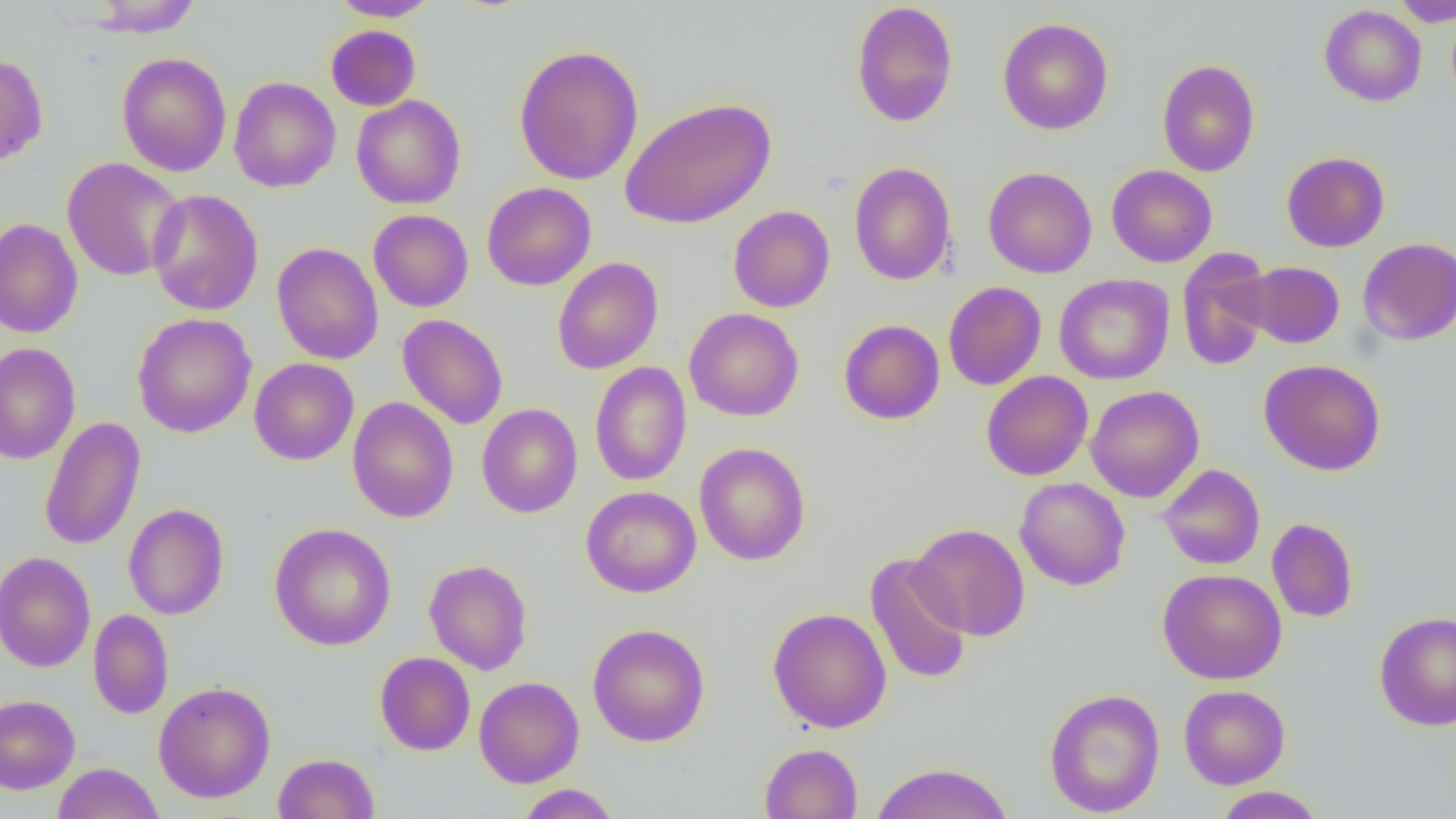

slide-level diagnosis = negative for blood parasites
image size = 1456×819 pixels
uninfected red blood cell locations = approximate bounding boxes as (x1, y1, x2, y2) in pixels: (86, 0, 202, 37), (329, 0, 440, 21), (1390, 0, 1456, 27), (850, 1, 958, 128), (1319, 4, 1427, 106), (997, 17, 1113, 135), (325, 25, 421, 111), (513, 44, 644, 185), (116, 51, 232, 177), (0, 53, 48, 169), (1157, 59, 1260, 177), (228, 77, 341, 192), (351, 95, 465, 210), (619, 96, 776, 230), (1281, 151, 1390, 252), (62, 157, 185, 281), (848, 161, 957, 286), (1106, 165, 1217, 267), (983, 166, 1097, 279), (482, 182, 596, 291), (147, 189, 263, 316), (728, 205, 835, 312), (368, 209, 473, 312), (0, 218, 84, 338), (1357, 237, 1456, 345), (271, 242, 384, 364), (1177, 248, 1275, 371), (552, 257, 663, 375), (1241, 261, 1344, 348), (1054, 274, 1175, 384), (943, 281, 1047, 390), (684, 307, 804, 422), (132, 313, 257, 438), (397, 314, 508, 429), (839, 319, 945, 425), (0, 342, 81, 465), (249, 358, 359, 465), (1258, 358, 1386, 476), (590, 361, 692, 486), (981, 371, 1093, 481), (1085, 385, 1204, 503), (347, 397, 459, 523), (476, 404, 583, 518), (39, 416, 146, 551), (694, 442, 811, 566), (1157, 464, 1265, 570), (1014, 477, 1130, 591), (580, 486, 701, 598), (123, 503, 229, 620), (1267, 517, 1359, 623), (269, 522, 396, 651), (909, 523, 1030, 641), (0, 551, 96, 672), (865, 553, 973, 685), (423, 559, 533, 675), (1157, 568, 1287, 685), (767, 607, 892, 733), (88, 609, 174, 719), (1374, 611, 1456, 731), (587, 623, 710, 747), (375, 651, 475, 755), (474, 676, 584, 788), (153, 681, 276, 803), (1178, 684, 1290, 789), (1044, 688, 1165, 816), (0, 694, 80, 793), (759, 742, 863, 819), (273, 752, 380, 818), (52, 762, 164, 819), (868, 762, 1016, 819), (515, 784, 621, 819), (1213, 786, 1325, 818)
modality = light microscopy
magnification = 1000x
field of view = one of a larger specimen
preparation = thin blood film